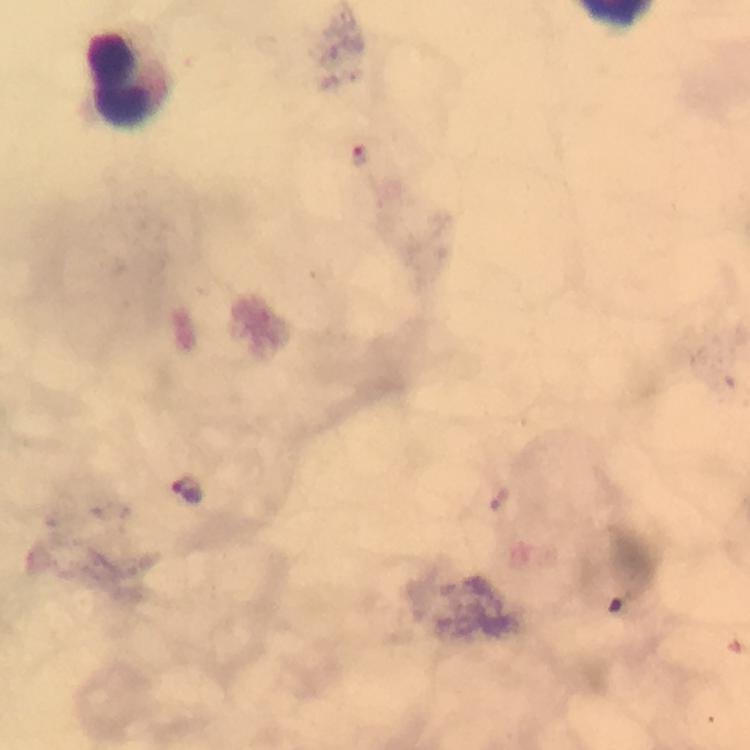

leukocyte locations = approximate centers as {x, y} in pixels: {124, 81}
preparation = thick blood film
capture = smartphone camera through the microscope
stain = Giemsa
context = from a diagnostic examination for malaria
image size = 750×750 pixels
immersion oil = used
magnification = 100x
cropped from = a single field of view
malaria parasite locations = approximate centers as {x, y} in pixels: {360, 154}, {186, 488}